Outline each Plasmodium falciparum-infected red blood cell.
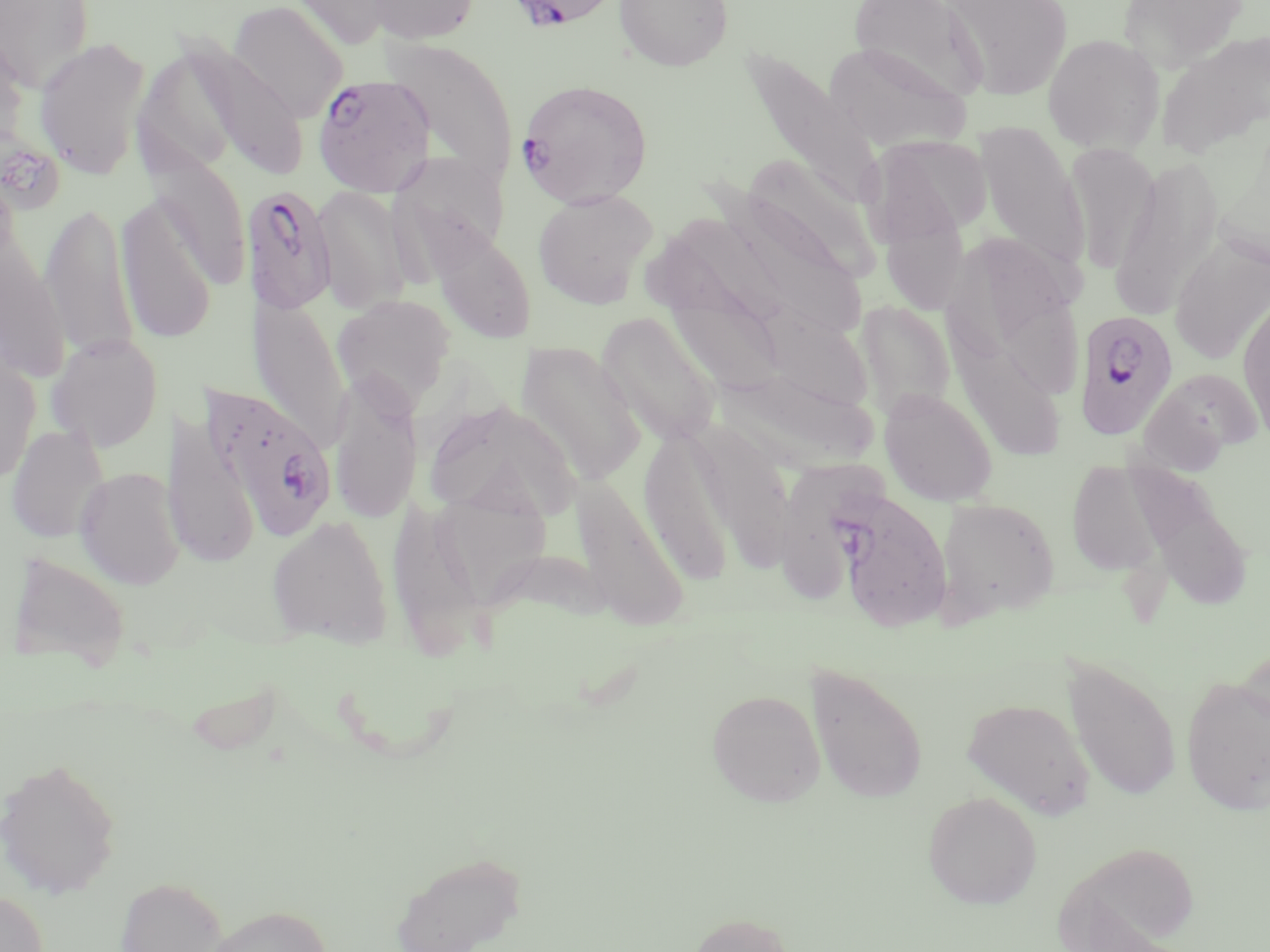
Approximate bounding boxes as (x1,y1)-(x2,y2) corner pairs in pixels.
Plasmodium falciparum-infected red blood cells: (512,2)-(610,37), (311,74)-(435,197), (516,78)-(654,208), (241,184)-(336,316), (1073,310)-(1180,441), (202,382)-(337,543), (834,488)-(953,632).

Uninfected red blood cell locations: (0,0)-(95,92), (286,0)-(400,50), (366,0)-(480,45), (614,0)-(733,72), (847,0)-(988,106), (943,0)-(1074,100), (1118,0)-(1250,72), (228,1)-(350,122), (0,26)-(32,170), (1155,29)-(1270,160), (1042,33)-(1165,154), (33,35)-(152,181), (383,35)-(518,185), (824,41)-(972,152), (186,42)-(309,181), (133,45)-(247,178), (738,47)-(885,211), (974,122)-(1088,277), (866,136)-(992,245), (1062,143)-(1160,276), (390,151)-(510,260), (146,152)-(252,288), (738,153)-(878,286), (1109,157)-(1224,320), (881,158)-(973,311), (710,181)-(869,343), (312,184)-(411,313), (533,189)-(658,308), (116,197)-(217,345), (40,201)-(139,364), (677,206)-(803,328), (0,208)-(70,383), (426,222)-(535,345), (985,231)-(1086,396), (641,234)-(773,363), (1170,234)-(1270,366), (1237,288)-(1270,445), (665,292)-(788,399), (251,293)-(351,451), (331,293)-(457,411), (946,297)-(1061,461), (760,298)-(880,411), (857,300)-(955,420), (596,312)-(723,448), (46,333)-(164,452), (517,343)-(647,485), (0,347)-(40,485), (723,365)-(877,472), (1140,368)-(1263,467), (328,376)-(422,527), (879,388)-(998,506), (425,400)-(582,525), (161,412)-(260,568), (7,424)-(109,543), (638,430)-(737,585), (1067,459)-(1165,576), (75,467)-(185,589), (1132,474)-(1256,612), (570,475)-(689,629), (428,485)-(553,611), (934,497)-(1060,622), (389,501)-(487,654), (266,514)-(394,648), (7,552)-(132,671), (1062,655)-(1181,804), (803,660)-(929,805), (1181,673)-(1270,816), (706,688)-(825,806), (961,697)-(1095,819), (0,756)-(123,899), (923,791)-(1042,909), (1053,841)-(1202,952), (388,849)-(527,952), (114,875)-(229,952), (0,888)-(48,952), (199,904)-(332,952), (685,911)-(798,952). Slide-level diagnosis: Plasmodium falciparum. One field of a larger specimen. Thin blood smear. Optical microscopy. Image is 1270×952 pixels. 1000x magnification. May-Grünwald-Giemsa-stained preparation.